Assess this cell for malaria.
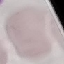

Uninfected.

capture = smartphone through the microscope eyepiece
preparation = thin blood smear
stain = Giemsa
image type = automatically extracted cell patch, resized to 64 × 64 pixels